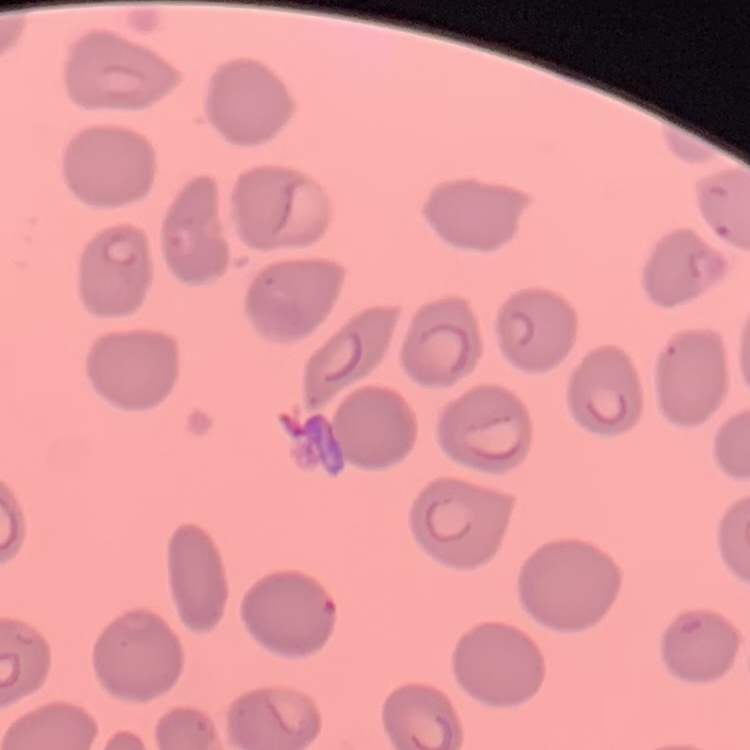 The erythrocytes exhibit no rouleaux formation. Thin blood smear. One tile cut from a larger photomicrograph. Field's or Giemsa stain.